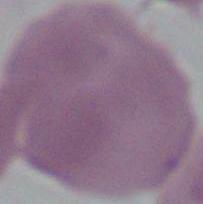

Summary:
  - Identification: erythrocyte
  - Magnification: 1000x
  - Modality: micrograph